Locate and identify every blood parasite.
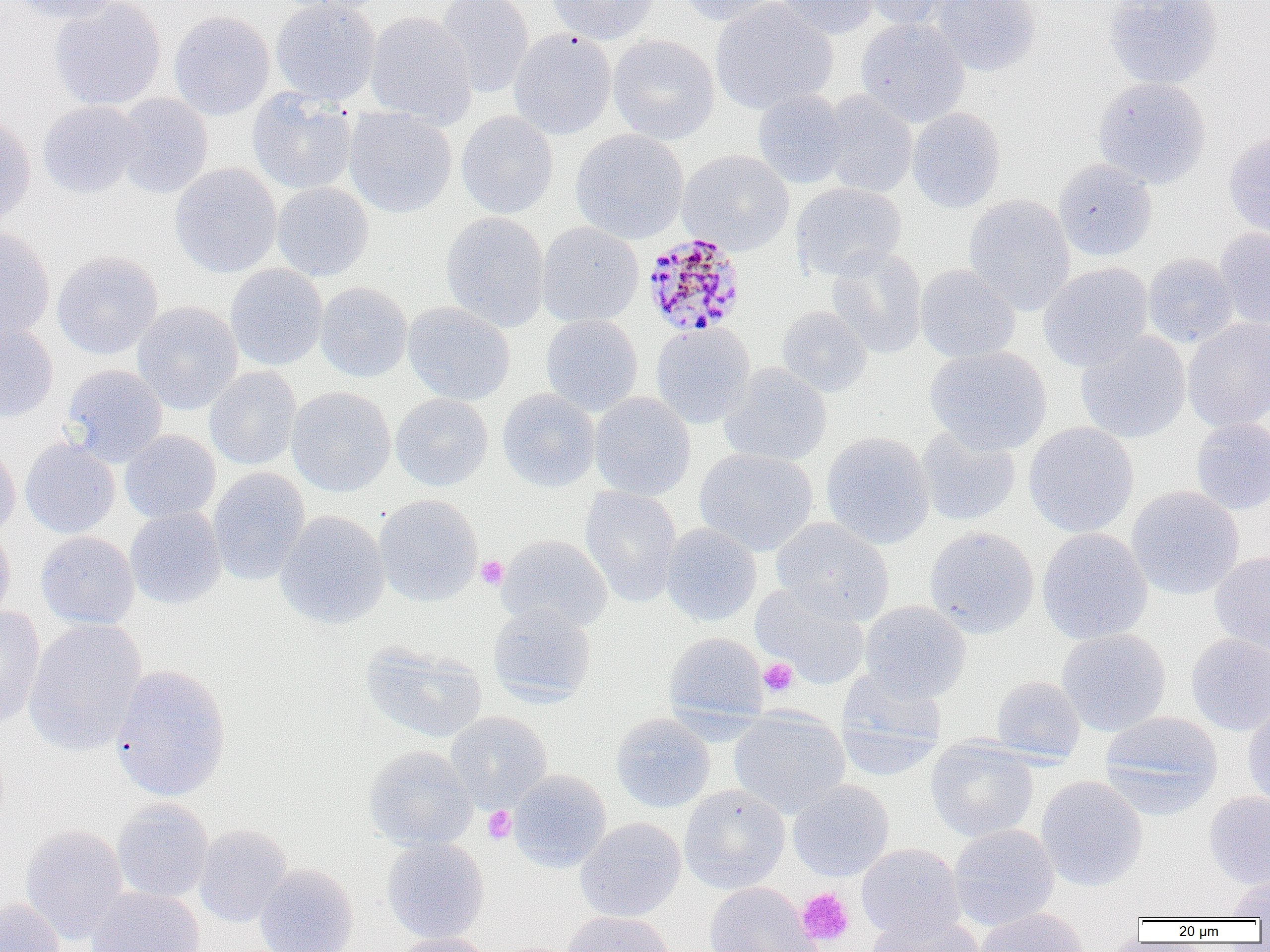

Approximate bounding boxes as (x1, y1, x2, y2) in pixels.
Plasmodium malariae-infected red blood cells: (642, 232, 747, 337).
No Plasmodium falciparum, Plasmodium ovale, Plasmodium vivax, Babesia divergens, or Trypanosoma brucei observed.

Summary:
  - Uninfected red blood cell locations: (8, 0, 124, 24), (268, 0, 393, 15), (270, 0, 381, 106), (435, 0, 534, 97), (548, 0, 659, 45), (674, 0, 782, 26), (709, 0, 837, 115), (775, 0, 879, 39), (859, 0, 964, 30), (931, 0, 1041, 77), (1103, 0, 1223, 89), (48, 1, 167, 111), (169, 10, 275, 120), (365, 12, 477, 127), (856, 18, 970, 127), (509, 29, 616, 140), (607, 34, 720, 145), (1092, 76, 1212, 189), (248, 88, 357, 195), (752, 89, 848, 188), (818, 90, 918, 198), (112, 93, 214, 199), (37, 100, 141, 198), (343, 107, 457, 218), (907, 108, 1006, 213), (456, 111, 558, 218), (0, 113, 35, 225), (570, 129, 689, 244), (1223, 131, 1270, 239), (677, 149, 794, 255), (1053, 158, 1158, 261), (169, 163, 282, 278), (272, 182, 374, 281), (791, 183, 906, 281), (963, 194, 1075, 315), (440, 211, 549, 333), (536, 222, 644, 327), (0, 227, 55, 341), (1215, 227, 1270, 331), (826, 246, 927, 358), (52, 250, 163, 360), (1143, 253, 1238, 348), (1038, 262, 1154, 372), (225, 264, 328, 371), (915, 264, 1021, 363), (315, 282, 412, 382), (403, 301, 515, 405), (132, 302, 243, 415), (776, 306, 872, 398), (541, 314, 643, 415), (1183, 318, 1270, 433), (651, 321, 755, 429), (0, 322, 58, 422), (1076, 331, 1191, 443), (925, 346, 1051, 456), (720, 363, 832, 467), (61, 364, 168, 467), (204, 366, 301, 471), (287, 387, 396, 497), (497, 389, 600, 492), (590, 392, 695, 500), (391, 393, 493, 491), (1191, 417, 1270, 515), (1024, 422, 1139, 537), (916, 426, 1021, 526), (119, 430, 221, 524), (821, 431, 934, 550), (21, 439, 120, 538), (0, 440, 21, 538), (694, 448, 819, 556), (208, 467, 310, 586), (580, 485, 683, 606), (1126, 486, 1244, 600), (374, 494, 482, 607), (125, 506, 227, 609), (275, 510, 389, 628), (771, 517, 894, 624), (0, 522, 15, 625), (660, 523, 762, 626), (924, 527, 1039, 639), (1037, 527, 1153, 645), (36, 531, 139, 629), (498, 534, 613, 632), (1209, 551, 1270, 655), (751, 583, 869, 689), (859, 600, 971, 702), (488, 603, 596, 704), (0, 607, 45, 728), (24, 618, 147, 756), (1057, 628, 1171, 736), (664, 632, 768, 723), (1186, 634, 1270, 735), (361, 641, 487, 742), (111, 664, 232, 802), (837, 669, 947, 780), (991, 675, 1085, 764), (1242, 704, 1270, 808), (729, 708, 850, 818), (1099, 710, 1223, 816), (446, 711, 552, 812), (611, 713, 715, 813), (926, 738, 1039, 842), (364, 745, 477, 850), (508, 770, 612, 872), (1036, 775, 1148, 891), (788, 780, 894, 881), (679, 784, 790, 894), (1204, 791, 1270, 889), (112, 799, 213, 903), (576, 817, 686, 922), (20, 824, 128, 943), (194, 824, 292, 927), (948, 824, 1060, 930), (382, 837, 489, 943), (856, 843, 965, 943), (255, 863, 359, 952), (1225, 875, 1270, 920), (704, 881, 819, 952), (85, 887, 205, 952), (0, 897, 67, 952), (975, 906, 1088, 952), (563, 911, 674, 952), (863, 915, 985, 952), (390, 934, 495, 952)
  - Platelet locations: (476, 556, 508, 590), (758, 658, 798, 696), (482, 806, 517, 844), (796, 888, 855, 946)
  - Slide-level diagnosis: Plasmodium malariae
  - Image size: 1270×952 pixels
  - Modality: light microscopy
  - Preparation: thin blood smear
  - Magnification: 1000x
  - Field of view: one of a larger specimen